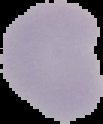
image_size: 103×124 pixels
preparation: thin blood film
result: no Plasmodium parasites seen
image_type: segmented cell region with the area outside set to black